Identify the blood parasite species.
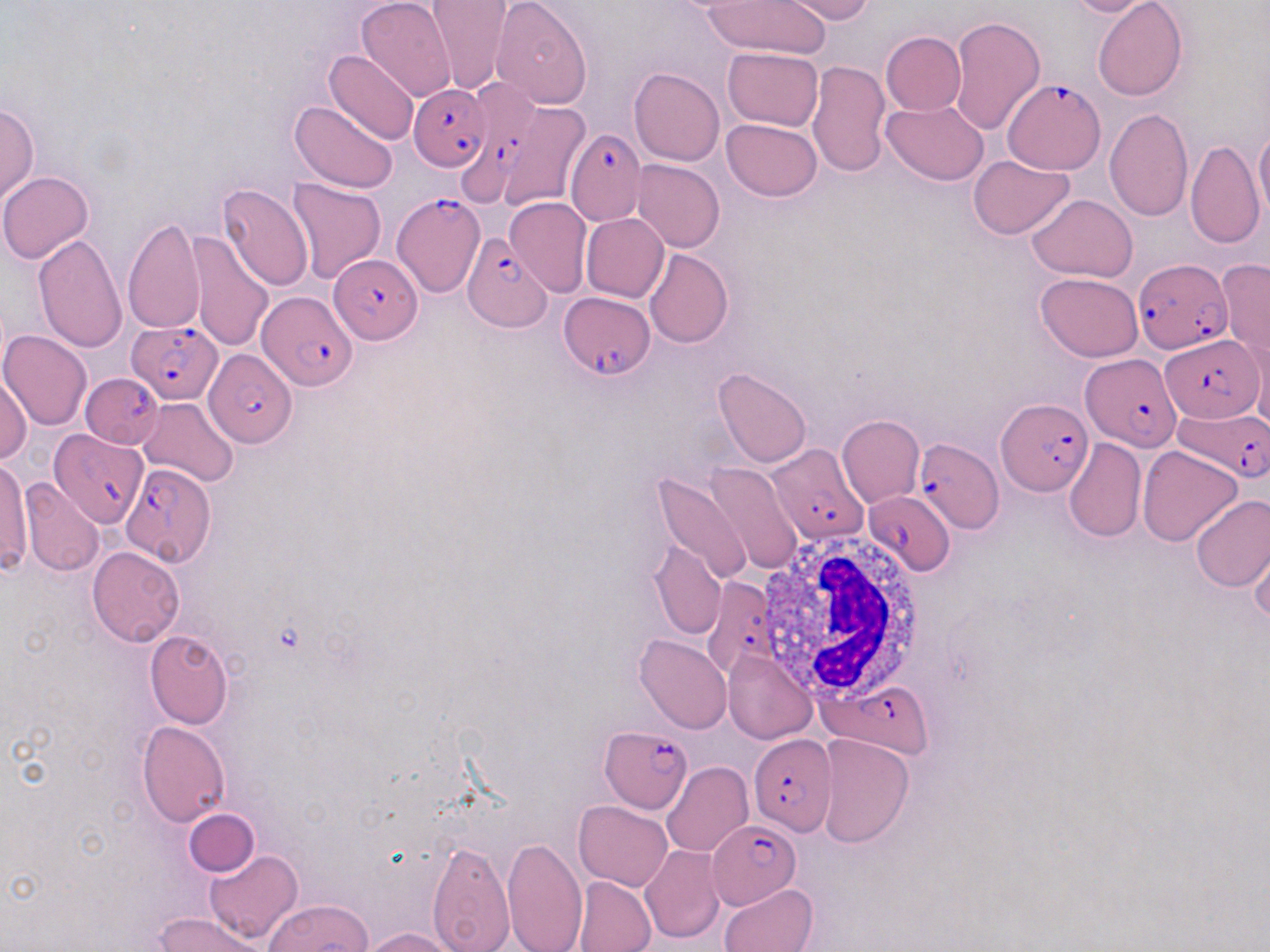

Plasmodium falciparum.

Summary:
  - Coordinate format: approximate bounding boxes as [x1, y1, x2, y2] in pixels
  - Plasmodium falciparum-infected red blood cell locations: [458, 79, 537, 208], [1005, 79, 1107, 178], [410, 83, 491, 170], [566, 129, 647, 224], [394, 194, 485, 295], [462, 234, 551, 331], [328, 254, 423, 344], [1132, 258, 1231, 356], [259, 290, 357, 393], [559, 291, 655, 380], [126, 321, 220, 403], [1162, 333, 1262, 420], [203, 349, 297, 448], [1080, 353, 1180, 451], [82, 371, 162, 448], [998, 399, 1093, 498], [1173, 405, 1270, 480], [51, 429, 146, 527], [912, 434, 1002, 533], [762, 443, 867, 544], [121, 463, 217, 566], [865, 488, 957, 575], [702, 576, 780, 678], [823, 681, 933, 756], [599, 724, 691, 814], [748, 734, 837, 836], [707, 820, 802, 906]
  - Uninfected red blood cell locations: [491, 0, 593, 109], [701, 0, 831, 59], [780, 0, 875, 23], [1058, 0, 1156, 18], [358, 1, 457, 104], [1093, 1, 1187, 101], [428, 2, 513, 96], [950, 15, 1045, 133], [881, 32, 966, 115], [722, 47, 823, 132], [324, 49, 420, 146], [807, 60, 892, 177], [629, 67, 725, 166], [883, 99, 989, 186], [289, 100, 399, 194], [508, 100, 589, 212], [0, 102, 40, 205], [1104, 108, 1193, 221], [721, 118, 822, 201], [1253, 126, 1270, 223], [1185, 140, 1264, 248], [968, 155, 1074, 239], [632, 159, 725, 252], [0, 172, 93, 263], [287, 177, 388, 284], [215, 183, 313, 290], [1027, 194, 1137, 281], [504, 198, 592, 296], [582, 213, 669, 303], [122, 217, 206, 334], [185, 231, 275, 353], [32, 233, 129, 353], [643, 248, 733, 348], [1217, 259, 1270, 368], [1035, 273, 1144, 361], [0, 330, 92, 431], [712, 367, 812, 467], [0, 374, 32, 464], [137, 396, 238, 486], [836, 414, 924, 508], [1063, 438, 1147, 544], [1137, 446, 1243, 547], [0, 461, 32, 573], [704, 462, 805, 574], [654, 471, 753, 585], [19, 477, 104, 577], [1190, 494, 1270, 593], [1248, 534, 1270, 628], [648, 538, 727, 640], [86, 546, 184, 646], [145, 630, 234, 729], [634, 633, 733, 734], [723, 649, 817, 744], [136, 721, 230, 825], [816, 733, 914, 846], [662, 762, 752, 857], [573, 801, 673, 891], [184, 809, 259, 878], [503, 837, 588, 952], [426, 840, 514, 950], [640, 846, 725, 943], [205, 850, 302, 945], [571, 875, 656, 952], [719, 883, 819, 952], [264, 899, 373, 951], [152, 911, 270, 952], [359, 926, 461, 951]
  - White blood cell locations: [754, 530, 929, 705]
  - Field of view: one of a larger specimen
  - Stain: May-Grünwald-Giemsa
  - Magnification: 1000x
  - Image size: 1270×952 pixels
  - Modality: optical microscopy
  - Preparation: thin blood film